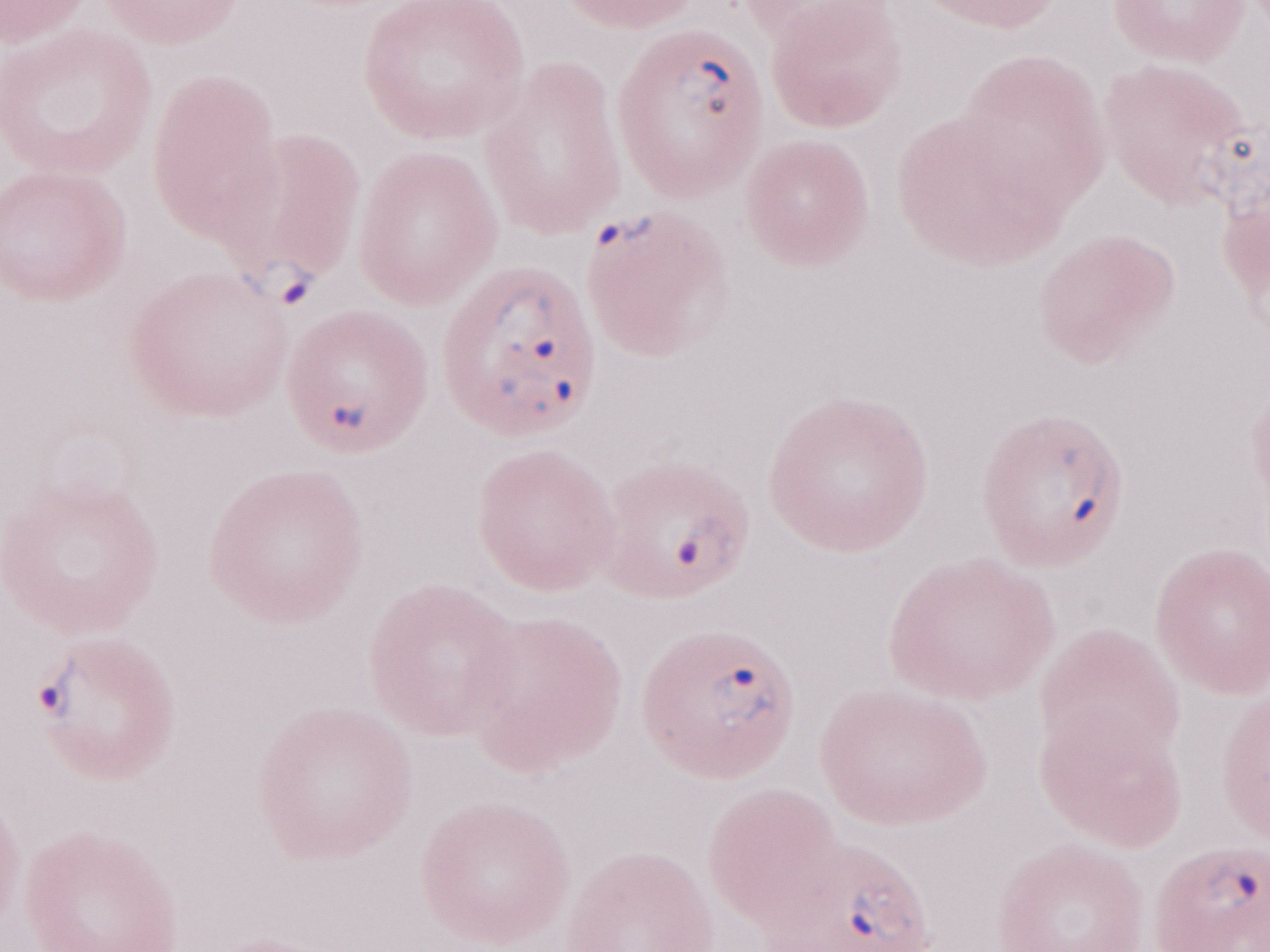 May-Grünwald-Giemsa stain. 1,000x magnification. Patient diagnosis: malaria infection. Olympus BX43 microscope and DP73 digital camera. Single field of view. Thin blood smear. Image is 1270×952 pixels.